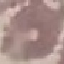
Malaria status: uninfected. Cell patch, automatically extracted from a larger field of view and resized to 64 × 64 pixels. Thin blood film. Photographed with a smartphone camera at the microscope eyepiece. Giemsa-stained preparation.